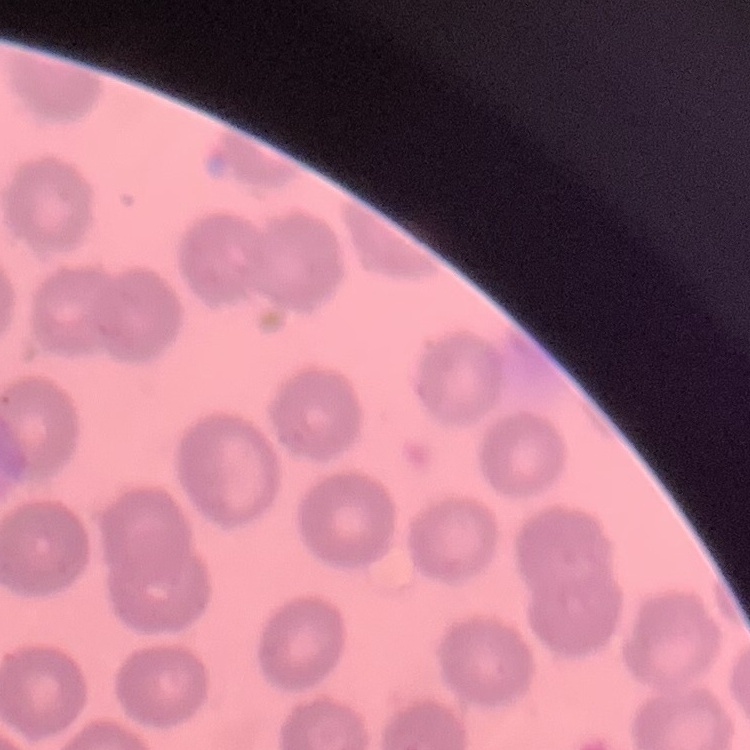
{
  "erythrocyte_morphology": "no rouleaux formation",
  "image_type": "square crop of a larger photomicrograph",
  "preparation": "thin blood smear",
  "stain": "Field's or Giemsa"
}